Name the parasite shown.
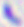

This is Toxoplasma gondii.

modality = micrograph
magnification = 400x